Name the parasite shown.
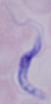
A trypanosome.

Summary:
  - Magnification: 1000x
  - Modality: photomicrograph